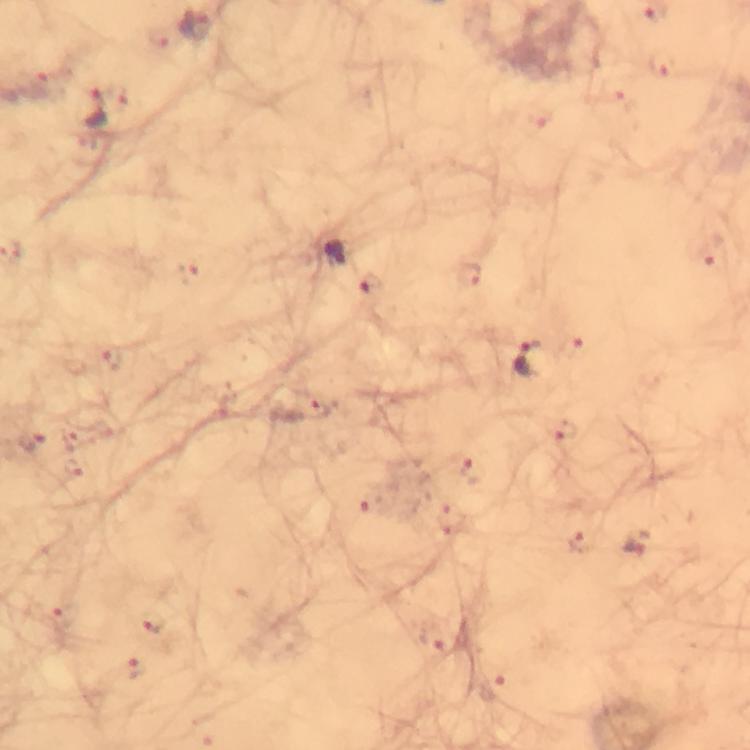

Approximate centers as {x, y} in pixels. Malaria parasite locations: {195, 23}, {661, 64}, {94, 107}, {711, 254}, {188, 272}, {469, 274}, {370, 285}, {573, 344}, {112, 358}, {531, 359}, {312, 405}, {561, 429}, {33, 439}, {75, 469}, {468, 469}, {451, 518}, {582, 540}, {637, 543}, {67, 616}, {155, 621}, {435, 637}, {136, 666}, {494, 689}. At 100x magnification. From a malaria diagnostic workup. Giemsa stain. Immersion oil applied. Cropped region of a single field of view. Thick blood smear. Image is 750×750 pixels. Photographed through the microscope with a smartphone camera.